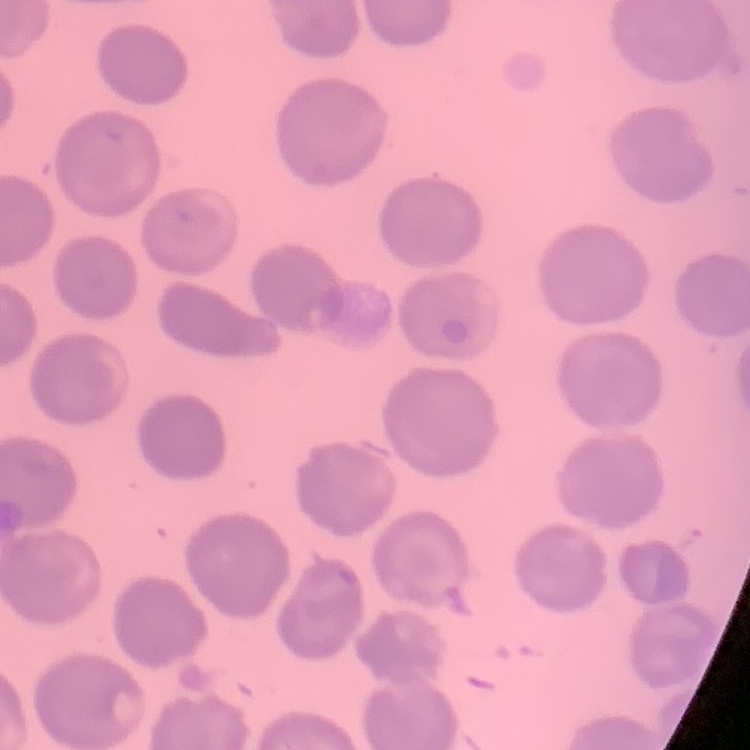

The erythrocytes exhibit no rouleaux formation. Thin blood film. Square crop of a larger photomicrograph. Field's or Giemsa stain.